Locate platelets.
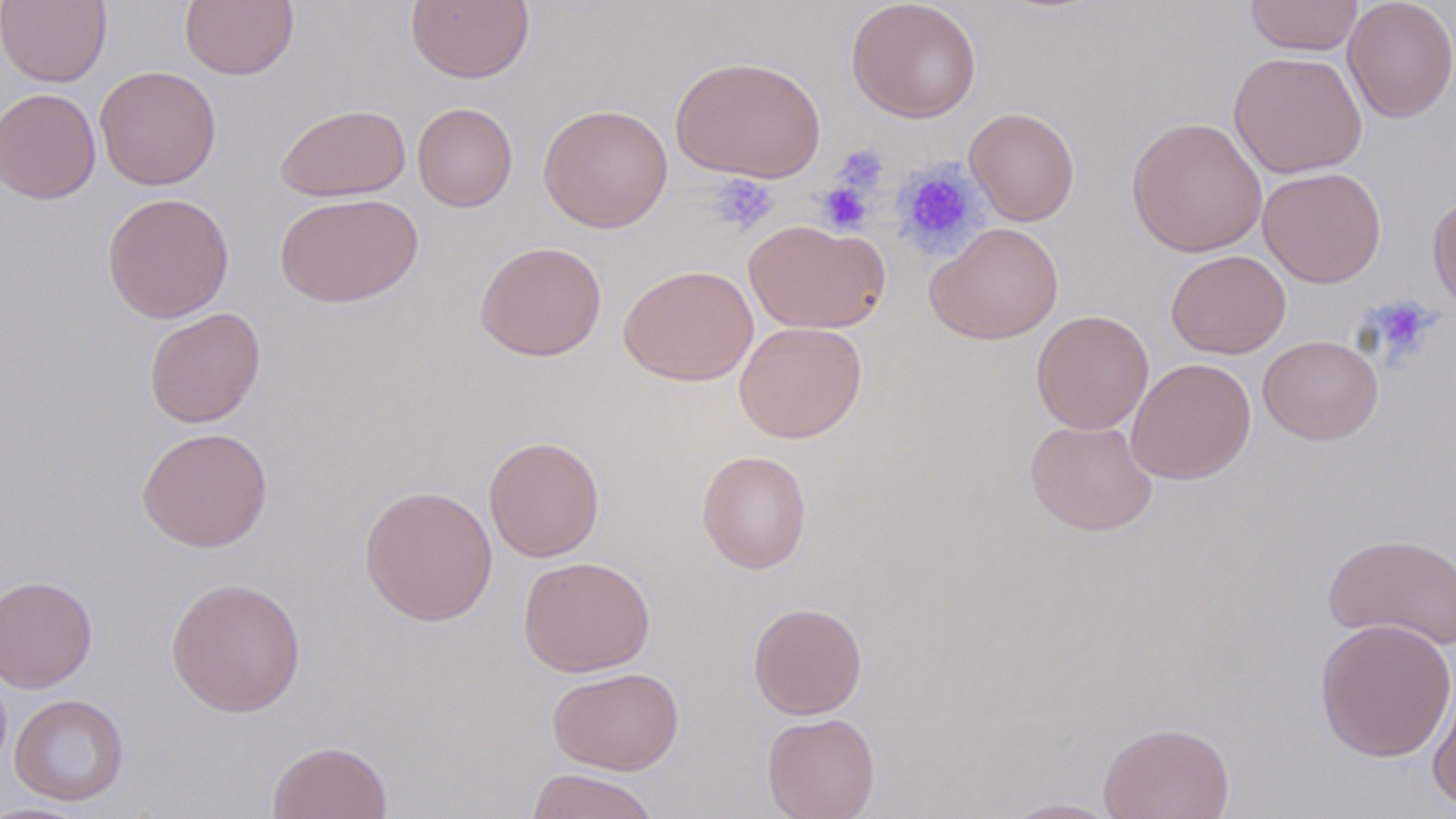
Approximate bounding boxes as (x1, y1, x2, y2) in pixels.
Platelets: (833, 145, 888, 195), (891, 159, 987, 258), (708, 173, 781, 236), (817, 181, 873, 235), (1366, 297, 1437, 362).

Uninfected red blood cell locations: (0, 0, 112, 87), (180, 0, 299, 80), (406, 0, 535, 84), (845, 0, 982, 123), (1245, 0, 1364, 56), (1342, 0, 1456, 123), (1229, 50, 1368, 179), (670, 55, 826, 183), (94, 65, 222, 190), (0, 88, 102, 205), (412, 102, 518, 212), (275, 103, 411, 202), (538, 103, 673, 233), (964, 106, 1080, 225), (1125, 116, 1268, 257), (1258, 166, 1386, 288), (101, 191, 235, 323), (275, 192, 424, 307), (1427, 192, 1456, 313), (744, 219, 890, 334), (925, 222, 1064, 345), (474, 240, 607, 361), (1166, 250, 1291, 359), (618, 265, 758, 386), (143, 307, 266, 428), (1031, 310, 1154, 435), (734, 321, 867, 443), (1258, 335, 1383, 445), (1125, 358, 1256, 485), (1025, 418, 1158, 536), (137, 426, 274, 552), (482, 436, 605, 563), (697, 450, 812, 574), (359, 484, 498, 627), (1323, 532, 1456, 651), (517, 555, 655, 677), (1, 574, 98, 693), (165, 576, 306, 717), (748, 602, 867, 720), (1313, 617, 1456, 762), (547, 666, 684, 775), (1428, 672, 1456, 810), (9, 693, 129, 806), (761, 712, 881, 819), (1097, 721, 1235, 819), (267, 740, 393, 819), (526, 768, 660, 819), (998, 797, 1127, 818), (0, 801, 97, 818). Slide-level diagnosis: no evidence of blood parasites. Thin blood smear. May-Grünwald-Giemsa-stained preparation. Single field of view. Image is 1456×819 pixels. Captured at 1000x magnification. Light microscopy.